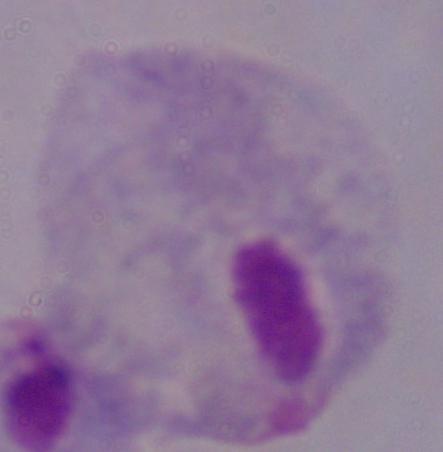
Micrograph. 1000x magnification. A trichomonad is seen.